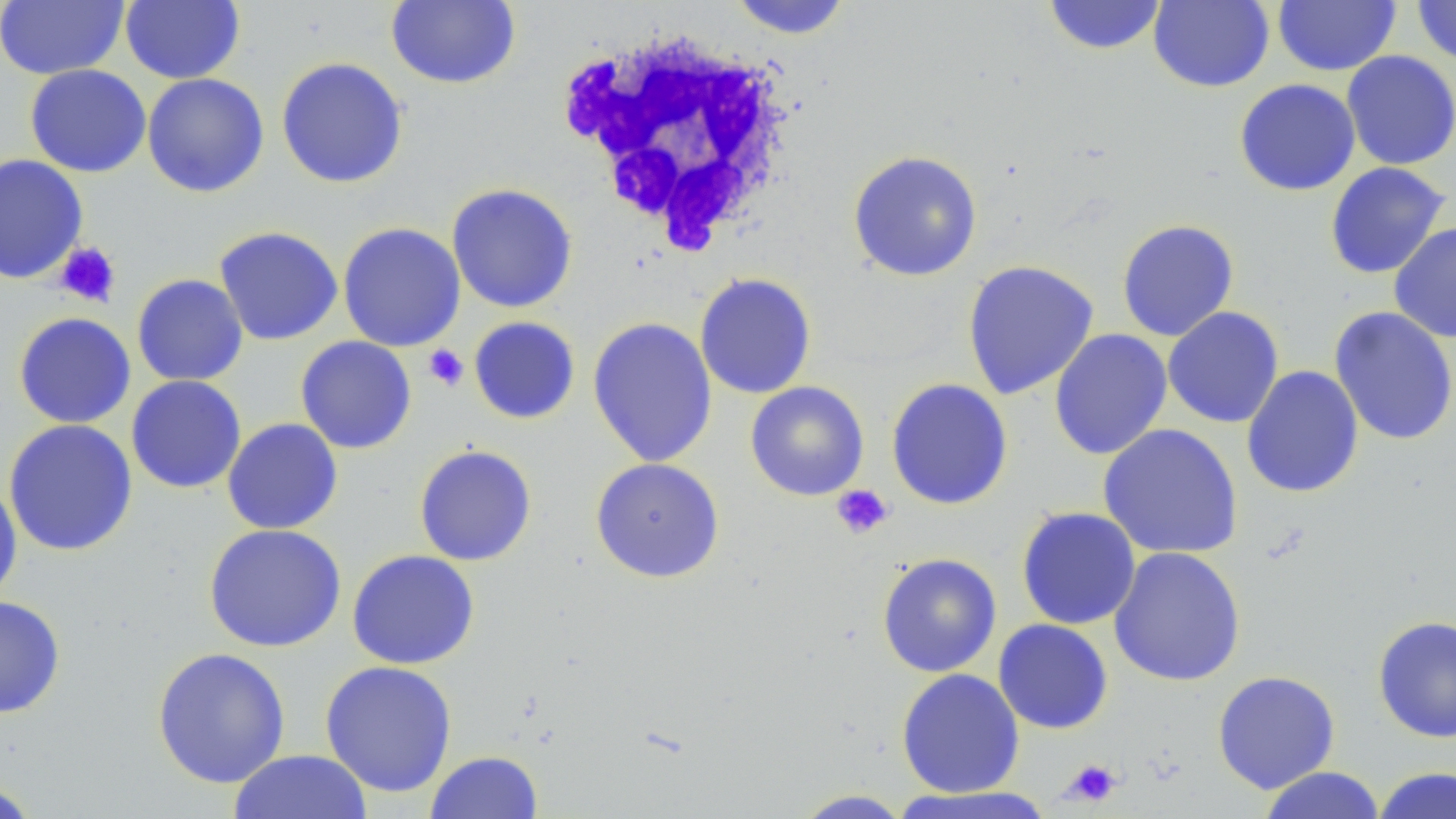 Approximate bounding boxes as (x1, y1, x2, y2) in pixels. Platelet locations: (54, 241, 121, 307), (423, 344, 469, 390), (831, 484, 893, 539), (1060, 758, 1123, 808). White blood cell locations: (559, 27, 800, 255). Uninfected red blood cell locations: (120, 0, 245, 84), (386, 0, 521, 90), (727, 0, 855, 39), (1042, 0, 1168, 56), (1148, 0, 1274, 92), (1412, 0, 1456, 67), (0, 1, 129, 80), (1272, 1, 1401, 76), (1340, 51, 1456, 171), (276, 57, 408, 188), (24, 64, 151, 178), (142, 73, 270, 198), (1234, 79, 1361, 196), (847, 150, 984, 282), (0, 153, 89, 285), (1324, 162, 1452, 279), (446, 183, 578, 314), (1116, 218, 1239, 342), (337, 222, 466, 352), (1388, 222, 1456, 343), (213, 225, 343, 346), (961, 260, 1099, 400), (694, 272, 817, 400), (131, 274, 249, 387), (1162, 306, 1284, 428), (1328, 306, 1456, 446), (13, 311, 136, 429), (468, 316, 581, 424), (587, 317, 718, 468), (1049, 329, 1173, 460), (295, 336, 417, 454), (1241, 365, 1365, 498), (125, 375, 247, 494), (886, 378, 1014, 511), (745, 381, 870, 501), (222, 417, 343, 534), (3, 419, 138, 557), (1097, 423, 1243, 559), (414, 444, 537, 566), (590, 457, 725, 583), (0, 478, 23, 606), (1016, 506, 1141, 630), (203, 523, 347, 653), (1108, 546, 1247, 687), (346, 549, 480, 670), (876, 552, 1002, 678), (0, 595, 67, 719), (1372, 615, 1456, 744), (993, 618, 1113, 734), (151, 646, 291, 789), (319, 660, 458, 798), (896, 668, 1025, 798), (1212, 670, 1340, 794), (228, 749, 373, 819), (425, 751, 543, 819), (1257, 766, 1387, 819), (1372, 766, 1456, 819), (0, 779, 42, 819), (891, 785, 1056, 818), (791, 789, 914, 818). Slide-level diagnosis: no evidence of blood parasites. One field of a larger specimen. Optical microscopy. Image is 1456×819 pixels. Thin blood film. May-Grünwald-Giemsa-stained preparation. Captured at 1000x magnification.